Mark where platelets are.
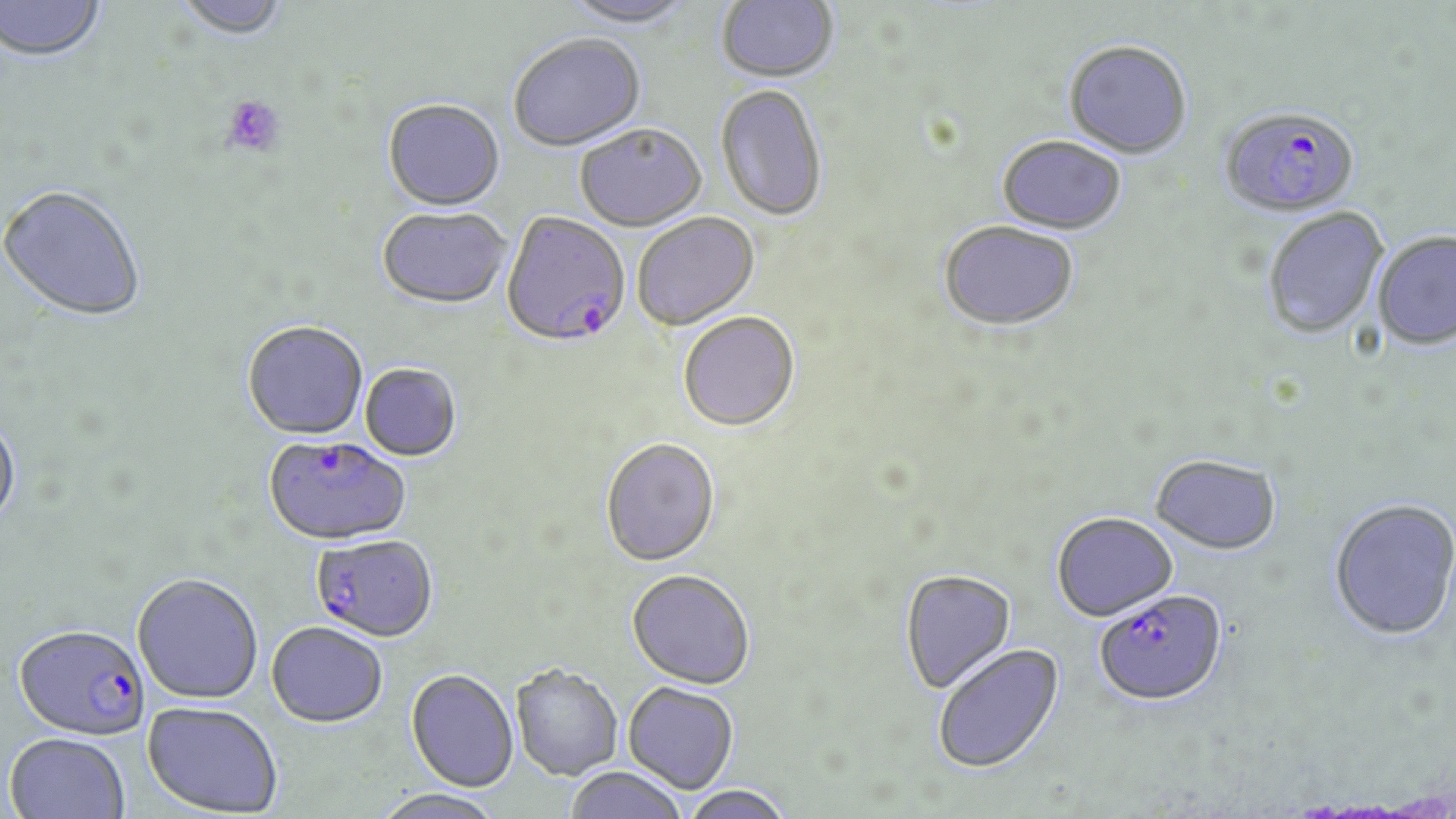
Approximate bounding boxes as [x1, y1, x2, y2] in pixels.
Platelets: [221, 94, 286, 158].

Summary:
  - Plasmodium falciparum-infected red blood cell locations: [1220, 106, 1360, 217], [502, 214, 632, 351], [264, 435, 410, 546], [311, 534, 438, 642], [1094, 591, 1227, 708], [14, 623, 150, 740]
  - Uninfected red blood cell locations: [0, 0, 107, 65], [173, 0, 291, 43], [560, 0, 696, 30], [716, 0, 840, 85], [509, 37, 646, 154], [1063, 42, 1192, 161], [716, 86, 828, 224], [382, 101, 505, 214], [575, 126, 707, 234], [996, 137, 1126, 236], [0, 186, 146, 323], [1262, 207, 1389, 339], [377, 209, 512, 312], [633, 214, 760, 332], [939, 223, 1079, 334], [1372, 231, 1456, 351], [678, 313, 800, 433], [242, 322, 369, 441], [360, 364, 462, 462], [0, 412, 22, 532], [600, 438, 720, 567], [1150, 455, 1281, 555], [1329, 498, 1456, 640], [1052, 513, 1178, 622], [627, 568, 755, 688], [900, 570, 1018, 695], [132, 573, 264, 703], [266, 621, 388, 726], [931, 643, 1066, 774], [510, 663, 623, 779], [406, 668, 519, 791], [623, 681, 739, 793], [142, 700, 283, 816], [4, 732, 131, 819], [563, 766, 689, 819], [680, 784, 794, 819], [371, 788, 505, 819]
  - Slide-level diagnosis: Plasmodium falciparum
  - Stain: May-Grünwald-Giemsa
  - Field of view: single
  - Image size: 1456×819 pixels
  - Modality: optical microscopy
  - Magnification: 1000x
  - Preparation: thin blood smear